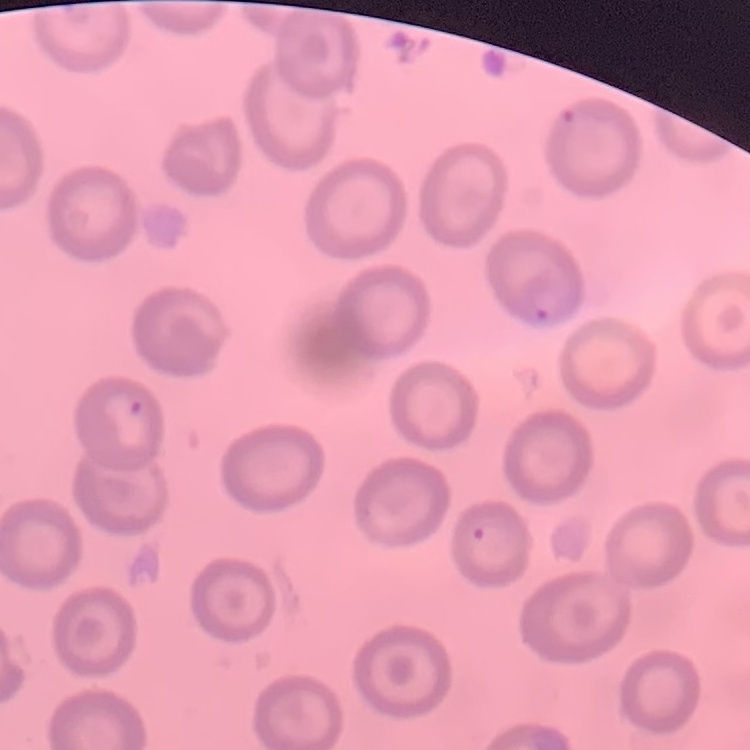

Summary:
  - Erythrocyte morphology: no rouleaux formation
  - Preparation: thin blood smear
  - Stain: Field's or Giemsa
  - Image type: one tile cut from a larger photomicrograph